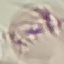
malaria status = uninfected
capture = smartphone through the microscope eyepiece
image type = automatically extracted cell patch, resized to 64 × 64 pixels
stain = Giemsa
preparation = thin blood smear